Identify the parasite.
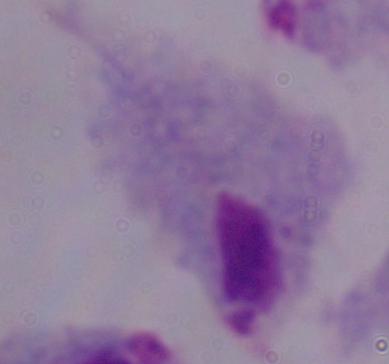
A trichomonad.

Micrograph. 1000x magnification.